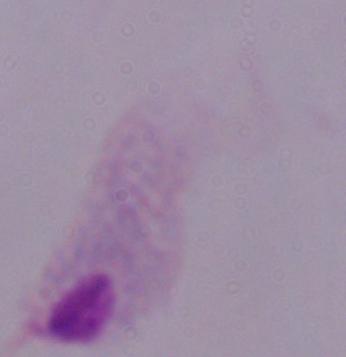

Summary:
  - Modality: micrograph
  - Identification: trichomonad
  - Magnification: 1000x